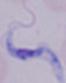
Summary:
  - Identification: trypanosome
  - Modality: photomicrograph
  - Magnification: 1000x